Locate every blood parasite and identify its species.
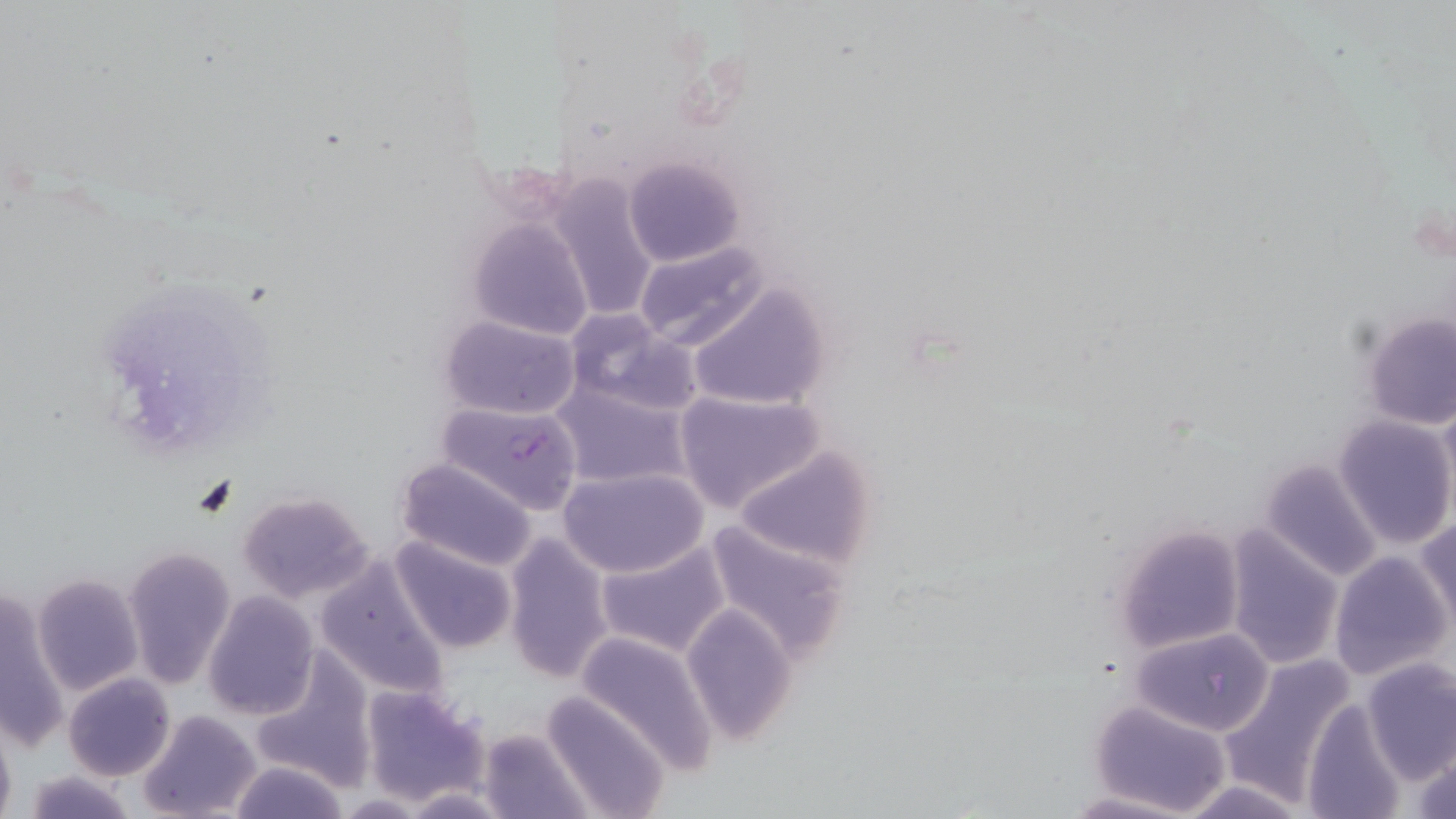
Approximate bounding boxes as [x1, y1, x2, y2] in pixels.
Plasmodium falciparum-infected red blood cells: [436, 399, 584, 512].
No Plasmodium ovale, Plasmodium malariae, Plasmodium vivax, Babesia divergens, or Trypanosoma brucei observed.

Summary:
  - Uninfected red blood cell locations: [620, 156, 743, 269], [544, 175, 660, 323], [467, 217, 595, 343], [633, 243, 770, 352], [684, 283, 831, 412], [566, 310, 696, 418], [1359, 310, 1455, 430], [439, 314, 583, 420], [552, 379, 693, 490], [672, 389, 826, 515], [1335, 415, 1455, 548], [733, 446, 879, 569], [1258, 456, 1384, 582], [394, 457, 539, 571], [558, 466, 707, 579], [236, 492, 376, 604], [1417, 517, 1455, 630], [701, 518, 853, 663], [1112, 523, 1248, 656], [1224, 527, 1344, 668], [503, 531, 615, 684], [390, 536, 519, 654], [595, 540, 732, 659], [121, 544, 236, 689], [1329, 551, 1451, 681], [314, 554, 454, 703], [31, 573, 143, 695], [0, 588, 68, 754], [203, 592, 319, 719], [682, 605, 799, 745], [1131, 626, 1276, 737], [575, 629, 719, 771], [250, 648, 376, 790], [1218, 653, 1358, 806], [1358, 657, 1455, 783], [64, 672, 174, 781], [359, 683, 488, 806], [541, 691, 671, 818], [1302, 696, 1408, 819], [1087, 700, 1233, 816], [138, 709, 260, 819], [0, 718, 16, 819], [476, 728, 591, 819], [1411, 744, 1456, 816], [226, 758, 351, 819], [22, 771, 139, 818], [1169, 776, 1311, 819], [401, 787, 513, 817], [1065, 790, 1194, 819]
  - Slide-level diagnosis: Plasmodium falciparum
  - Modality: light microscopy
  - Magnification: 1000x
  - Preparation: thin blood film
  - Stain: May-Grünwald-Giemsa
  - Field of view: one of a larger specimen
  - Image size: 1456×819 pixels